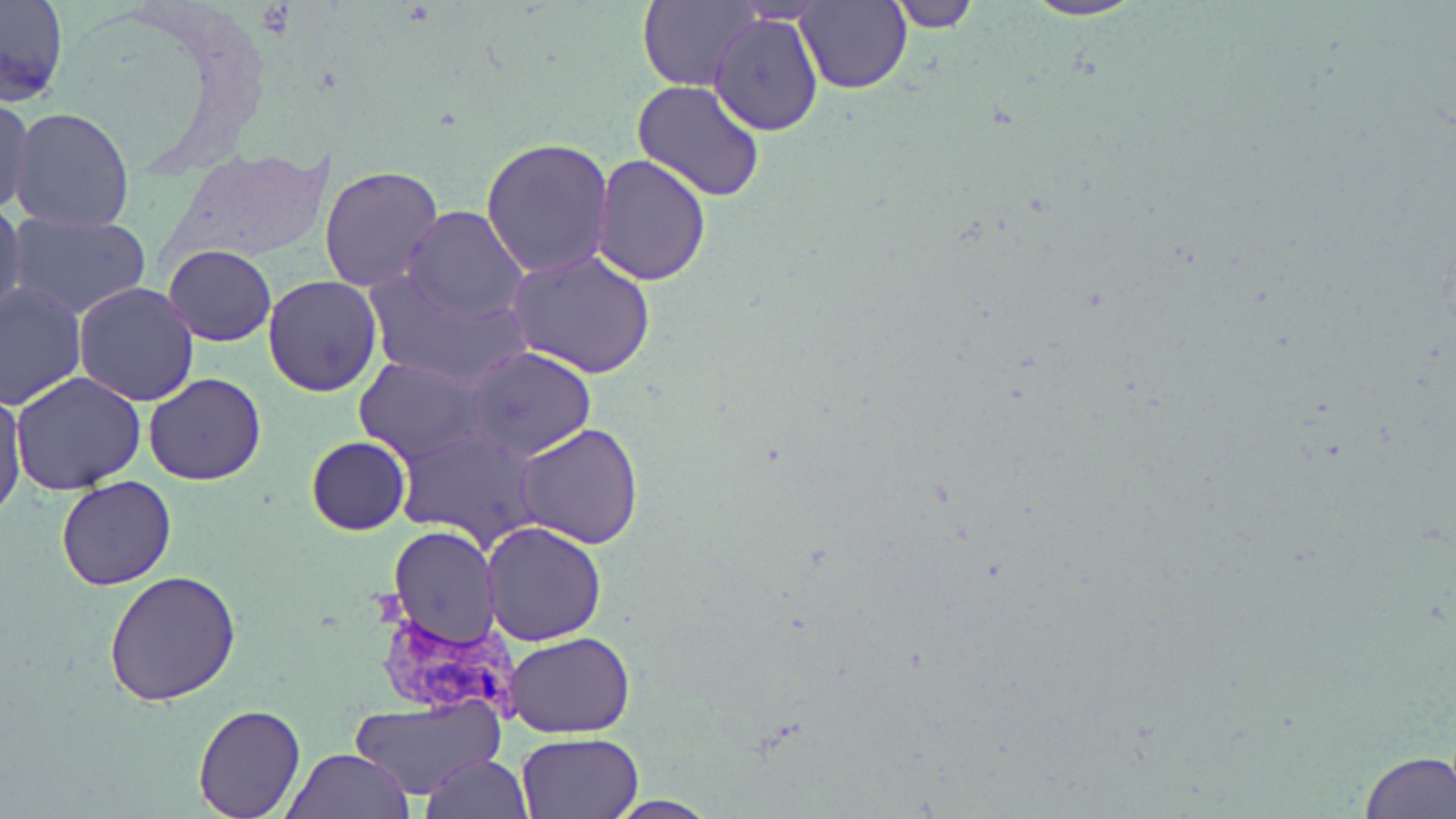
slide_level_diagnosis: Plasmodium vivax
magnification: 1000x
modality: light microscopy
preparation: thin blood smear
plasmodium_vivax_infected_red_blood_cell_locations: 'approximate bounding boxes as [x1, y1, x2, y2] in pixels: [371, 607, 522, 723]'
image_size: 1456×819 pixels
field_of_view: single
stain: May-Grünwald-Giemsa
uninfected_red_blood_cell_locations: 'approximate bounding boxes as [x1, y1, x2, y2] in pixels: [0, 0, 69, 103], [639, 0, 763, 92], [884, 0, 980, 31], [1021, 0, 1148, 22], [795, 3, 911, 92], [709, 11, 824, 137], [631, 80, 768, 205], [1, 95, 36, 220], [9, 107, 135, 232], [481, 137, 614, 279], [170, 147, 337, 265], [591, 154, 711, 286], [319, 166, 444, 291], [0, 201, 27, 325], [400, 206, 528, 323], [7, 213, 154, 319], [164, 245, 276, 346], [506, 249, 658, 379], [367, 267, 527, 388], [262, 275, 382, 396], [0, 281, 85, 412], [74, 282, 202, 406], [466, 346, 597, 462], [354, 356, 486, 464], [11, 372, 146, 496], [145, 372, 266, 486], [0, 390, 27, 518], [513, 423, 645, 550], [395, 427, 541, 551], [306, 436, 410, 535], [56, 475, 177, 590], [480, 521, 607, 646], [388, 527, 501, 648], [101, 567, 245, 706], [505, 631, 634, 738], [350, 696, 503, 801], [191, 702, 307, 819], [515, 732, 643, 818], [284, 749, 416, 818], [1358, 750, 1454, 818], [422, 753, 533, 819], [604, 796, 717, 817]'